Report the malaria status of this cell.
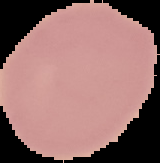

It is uninfected.

image type = segmented cell region with the area outside set to black
preparation = thin blood film
image size = 160×163 pixels